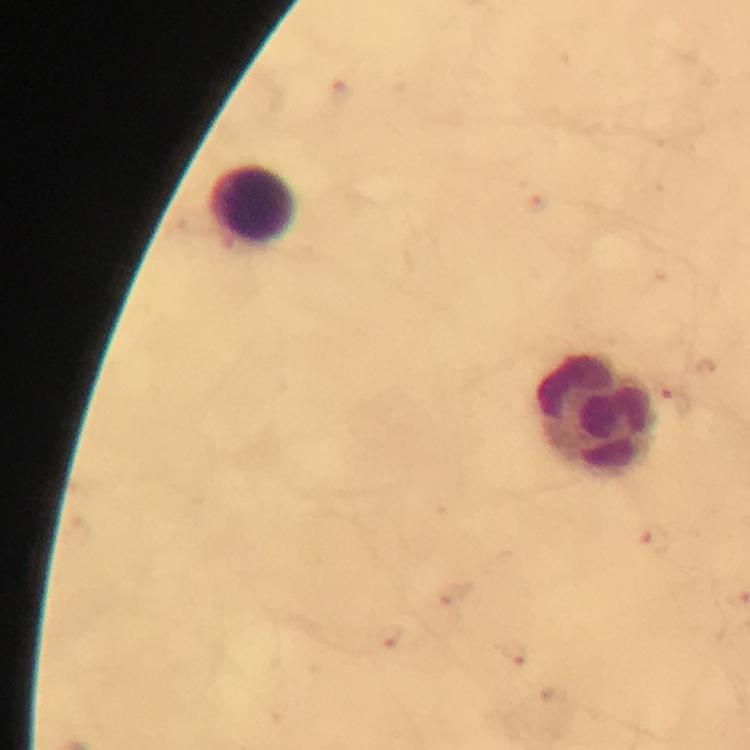
immersion oil = used
stain = Giemsa
leukocyte locations = approximate centers as (x, y) in pixels: (254, 204), (596, 414)
capture = smartphone camera through the microscope
image size = 750×750 pixels
magnification = 100x
context = from a malaria diagnostic workup
cropped from = one field of view
preparation = thick blood film
malaria parasite locations = approximate centers as (x, y) in pixels: (341, 93), (675, 398), (653, 539), (456, 597), (389, 637), (512, 656)